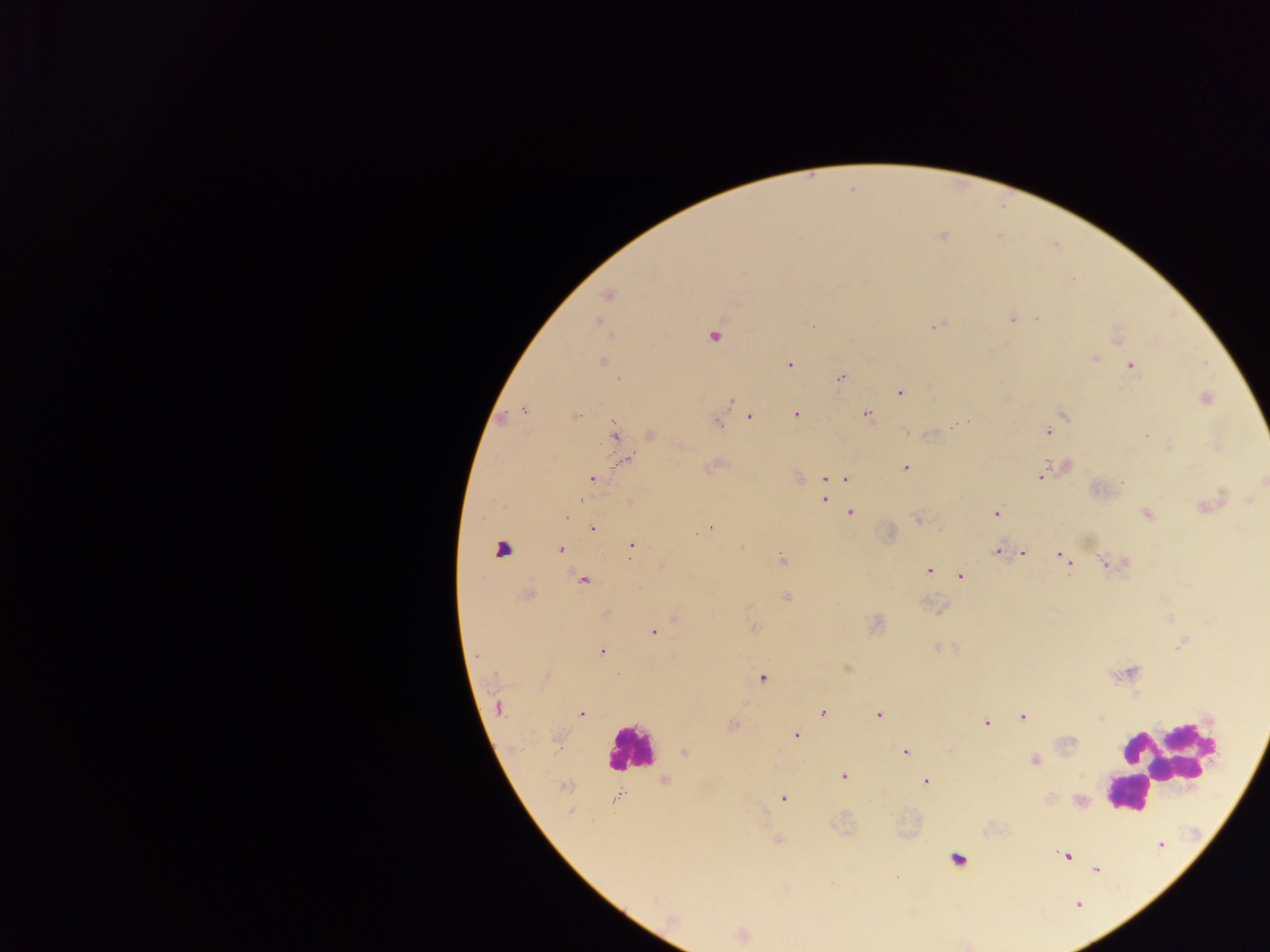
Approximate centers as {x, y} in pixels. Leukocyte locations: {501, 548}, {629, 749}, {1164, 763}, {1132, 793}, {956, 859}. Plasmodium parasite locations: {941, 235}, {607, 295}, {1011, 317}, {1037, 317}, {597, 321}, {935, 325}, {713, 335}, {1117, 337}, {1093, 358}, {601, 360}, {789, 364}, {1131, 366}, {840, 377}, {900, 392}, {1203, 398}, {524, 410}, {867, 413}, {796, 414}, {574, 416}, {749, 416}, {502, 419}, {717, 422}, {960, 422}, {1048, 431}, {650, 434}, {615, 435}, {1146, 435}, {680, 445}, {1169, 447}, {624, 460}, {1064, 465}, {713, 466}, {905, 467}, {838, 475}, {1041, 477}, {592, 478}, {796, 478}, {823, 478}, {846, 478}, {824, 489}, {823, 499}, {1250, 500}, {581, 501}, {629, 501}, {1209, 505}, {568, 512}, {1146, 512}, {850, 513}, {996, 513}, {566, 517}, {917, 518}, {592, 528}, {710, 528}, {631, 545}, {559, 549}, {997, 551}, {1022, 552}, {1061, 555}, {782, 560}, {1067, 561}, {1107, 564}, {661, 565}, {929, 569}, {959, 576}, {584, 579}, {525, 594}, {787, 597}, {604, 614}, {674, 618}, {753, 627}, {653, 632}, {1184, 640}, {937, 646}, {601, 651}, {1127, 673}, {762, 676}, {1137, 694}, {498, 708}, {823, 712}, {581, 713}, {878, 715}, {1023, 716}, {1100, 717}, {986, 723}, {732, 724}, {796, 735}, {557, 738}, {905, 751}, {685, 752}, {1035, 759}, {843, 776}, {665, 781}, {925, 781}, {565, 786}, {618, 797}, {783, 797}, {1080, 800}, {570, 812}, {777, 839}, {1067, 855}, {1096, 868}, {741, 935}. Mobile-phone photograph taken through the microscope. Sample from Ghana. One field of view. Thick blood smear. Image is 1270×952 pixels.